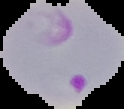

image type = segmented cell region on a black background
preparation = thin blood film
image size = 124×109 pixels
result = Plasmodium parasites identified